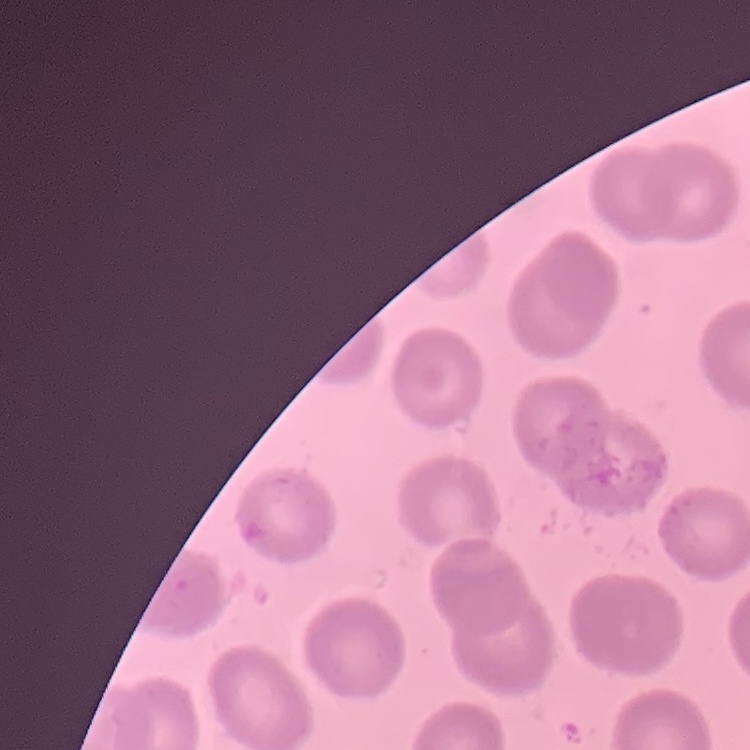

{
  "erythrocyte_morphology": "no rouleaux formation",
  "preparation": "thin peripheral smear",
  "stain": "Field's or Giemsa",
  "image_type": "one tile cut from a larger photomicrograph"
}